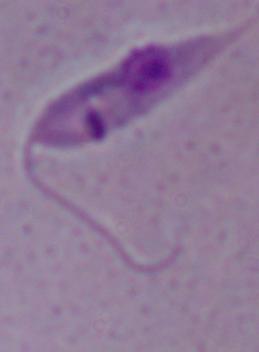

Summary:
  - Modality: micrograph
  - Identification: Leishmania
  - Magnification: 1000x